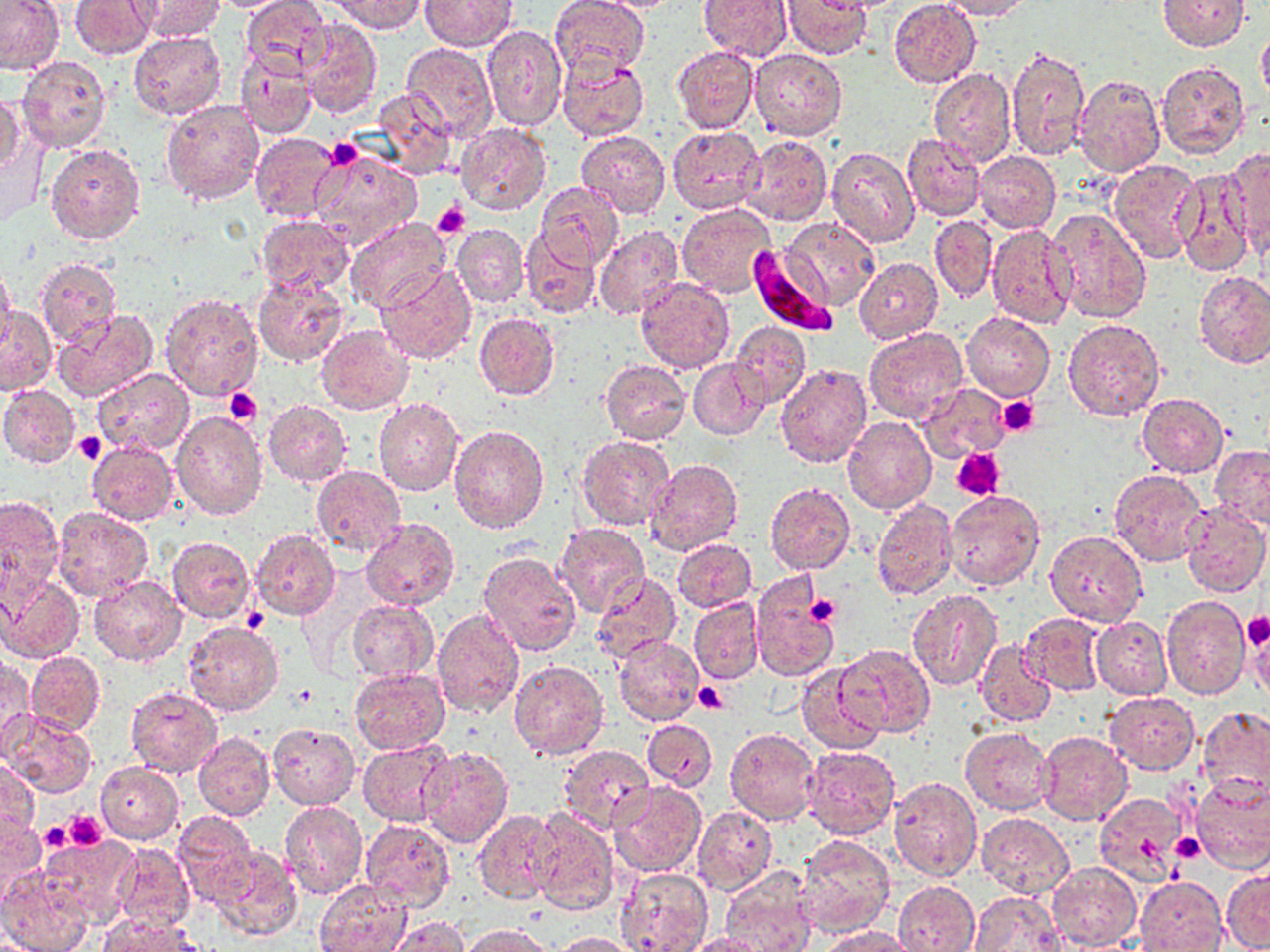 Approximate bounding boxes as (x1, y1, x2, y2) in pixels. Plasmodium falciparum-infected red blood cell locations: (746, 245, 837, 336). Uninfected red blood cell locations: (0, 0, 67, 75), (72, 0, 156, 59), (131, 0, 225, 41), (240, 0, 335, 80), (329, 0, 426, 34), (421, 0, 516, 50), (550, 0, 648, 78), (590, 0, 686, 13), (699, 0, 793, 62), (888, 0, 980, 87), (938, 0, 1032, 21), (1157, 0, 1248, 52), (783, 1, 873, 58), (703, 3, 871, 71), (297, 20, 383, 118), (481, 24, 567, 133), (1256, 28, 1270, 103), (128, 31, 228, 120), (401, 43, 497, 139), (1004, 44, 1090, 162), (672, 46, 759, 135), (749, 47, 846, 140), (233, 51, 318, 140), (558, 55, 648, 142), (17, 56, 111, 153), (1157, 61, 1249, 159), (928, 69, 1018, 168), (1073, 71, 1165, 177), (372, 87, 458, 181), (1, 91, 25, 176), (160, 98, 264, 205), (455, 122, 551, 217), (668, 126, 765, 214), (576, 129, 669, 219), (249, 132, 345, 223), (2, 133, 46, 228), (902, 133, 986, 221), (738, 134, 832, 225), (44, 142, 146, 245), (826, 146, 920, 247), (1227, 147, 1270, 251), (311, 148, 422, 252), (975, 151, 1059, 233), (1108, 159, 1201, 263), (1171, 167, 1257, 277), (534, 182, 623, 270), (675, 202, 777, 298), (1046, 208, 1152, 324), (255, 214, 354, 295), (930, 215, 998, 303), (782, 216, 880, 312), (342, 217, 452, 314), (452, 223, 530, 308), (985, 223, 1075, 328), (594, 225, 683, 320), (520, 231, 601, 318), (854, 256, 943, 343), (36, 258, 121, 347), (0, 262, 17, 352), (375, 265, 475, 364), (1195, 273, 1270, 370), (252, 274, 351, 366), (635, 278, 736, 374), (158, 292, 263, 401), (0, 305, 57, 396), (50, 309, 159, 405), (474, 312, 560, 400), (962, 313, 1055, 400), (1062, 318, 1167, 422), (729, 321, 812, 409), (315, 325, 415, 413), (863, 327, 969, 425), (601, 359, 690, 445), (689, 359, 770, 440), (774, 363, 872, 468), (92, 368, 194, 456), (918, 383, 1009, 463), (0, 384, 81, 467), (1136, 392, 1229, 478), (262, 398, 353, 487), (374, 399, 464, 498), (170, 409, 267, 521), (843, 415, 936, 514), (449, 425, 551, 534), (578, 434, 677, 532), (87, 440, 180, 526), (1210, 445, 1270, 527), (645, 459, 742, 556), (311, 465, 407, 559), (1109, 470, 1210, 566), (765, 483, 855, 574), (944, 490, 1045, 592), (0, 495, 65, 602), (871, 497, 957, 601), (1181, 503, 1269, 598), (52, 506, 152, 600), (360, 518, 459, 612), (554, 523, 651, 617), (250, 530, 342, 621), (1045, 530, 1147, 627), (167, 535, 257, 624), (672, 538, 757, 612), (478, 552, 582, 656), (591, 571, 680, 662), (0, 574, 85, 662), (88, 575, 186, 666), (751, 575, 838, 684), (908, 588, 1003, 690), (1161, 595, 1251, 699), (688, 597, 763, 685), (347, 599, 437, 682), (432, 606, 526, 716), (1019, 611, 1105, 695), (1091, 616, 1172, 700), (1249, 618, 1269, 703), (183, 621, 284, 717), (612, 634, 705, 727), (977, 641, 1054, 725), (836, 642, 934, 738), (26, 652, 104, 736), (1, 656, 34, 756), (508, 660, 610, 761), (797, 663, 888, 755), (349, 667, 450, 754), (126, 687, 223, 779), (1104, 693, 1200, 774), (1197, 705, 1270, 796), (2, 710, 99, 798), (642, 719, 718, 791), (266, 723, 360, 810), (725, 726, 819, 824), (960, 726, 1055, 815), (193, 731, 276, 821), (1037, 732, 1131, 826), (357, 740, 455, 826), (800, 744, 901, 839), (558, 745, 655, 833), (417, 747, 514, 849), (0, 756, 39, 839), (95, 762, 184, 844), (1188, 773, 1270, 872), (887, 777, 983, 880), (610, 783, 707, 878), (1094, 793, 1185, 884), (279, 801, 368, 900), (691, 805, 777, 896), (531, 808, 619, 915), (473, 809, 560, 905), (172, 810, 256, 904), (976, 813, 1075, 898), (0, 814, 45, 902), (361, 818, 454, 912), (795, 834, 895, 937), (38, 839, 140, 927), (115, 843, 194, 931), (213, 846, 303, 941), (1048, 861, 1142, 949), (720, 865, 817, 952), (1222, 865, 1270, 951), (0, 867, 92, 952), (615, 867, 714, 952), (1136, 876, 1227, 951), (315, 880, 411, 952), (894, 880, 981, 952), (967, 891, 1067, 951), (100, 915, 204, 952), (389, 916, 468, 952), (461, 924, 553, 952), (819, 925, 914, 952), (550, 931, 641, 951), (677, 933, 767, 952). Platelet locations: (324, 137, 363, 171), (432, 201, 469, 239), (224, 388, 262, 425), (997, 396, 1041, 437), (73, 432, 107, 465), (954, 450, 1004, 498), (803, 594, 841, 624), (1242, 613, 1270, 649), (694, 682, 728, 713), (292, 685, 318, 706), (65, 810, 107, 850), (39, 821, 72, 853), (1171, 832, 1202, 860). Slide-level diagnosis: Plasmodium falciparum. Optical microscopy. Thin blood film. Single field of view. May-Grünwald-Giemsa stain. Image is 1270×952 pixels. Captured at 1000x magnification.